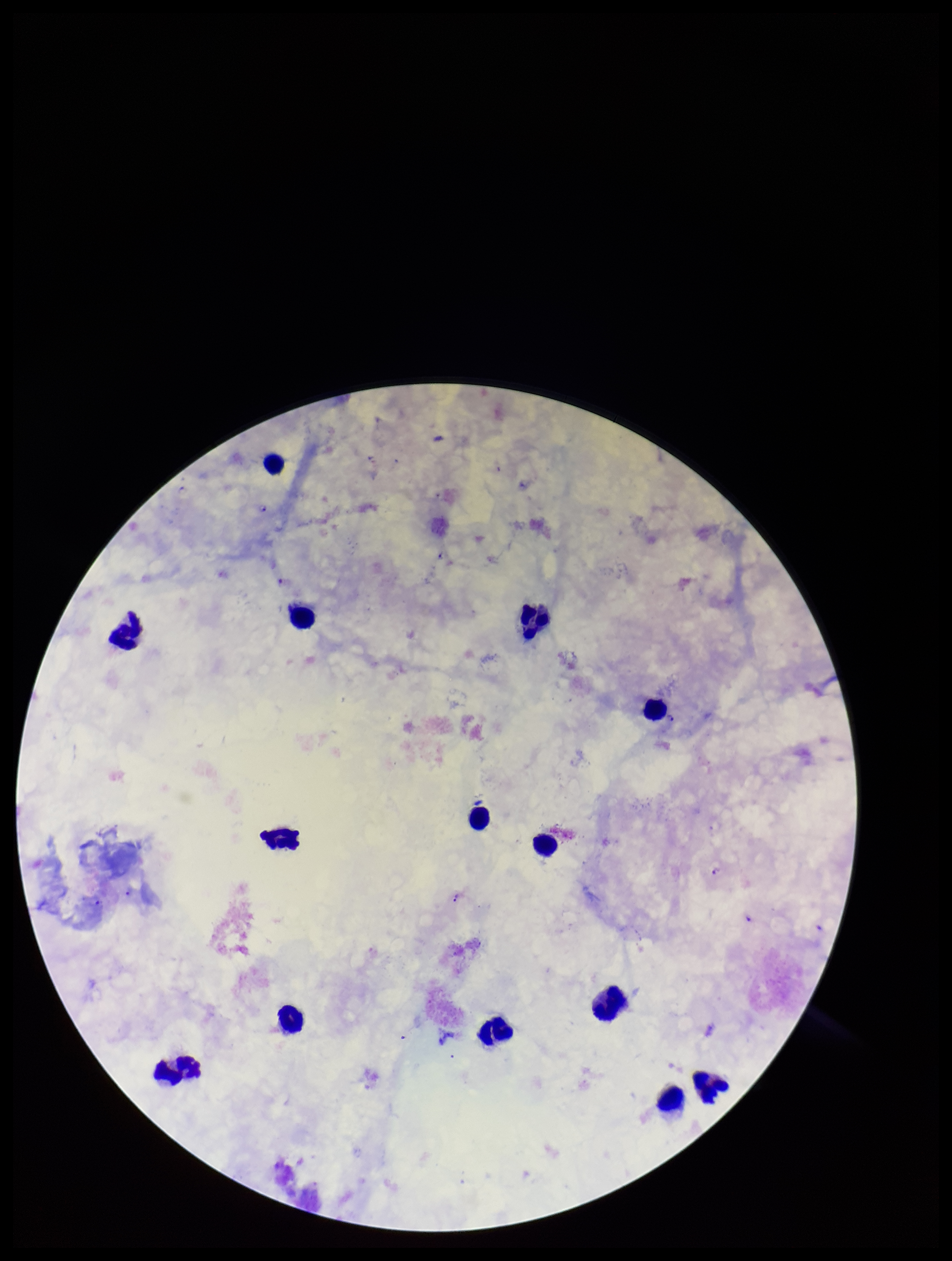
Patient malaria status: infected. Image is 952×1261 pixels. Parasite count: 8. Plasmodium parasites: detected. Giemsa stain. Single field of view. Species reported for this patient: Plasmodium falciparum. Leukocyte count: 14. Smartphone photograph taken through the eyepiece of a microscope. Preparation: thick smear.